State the blood parasite species.
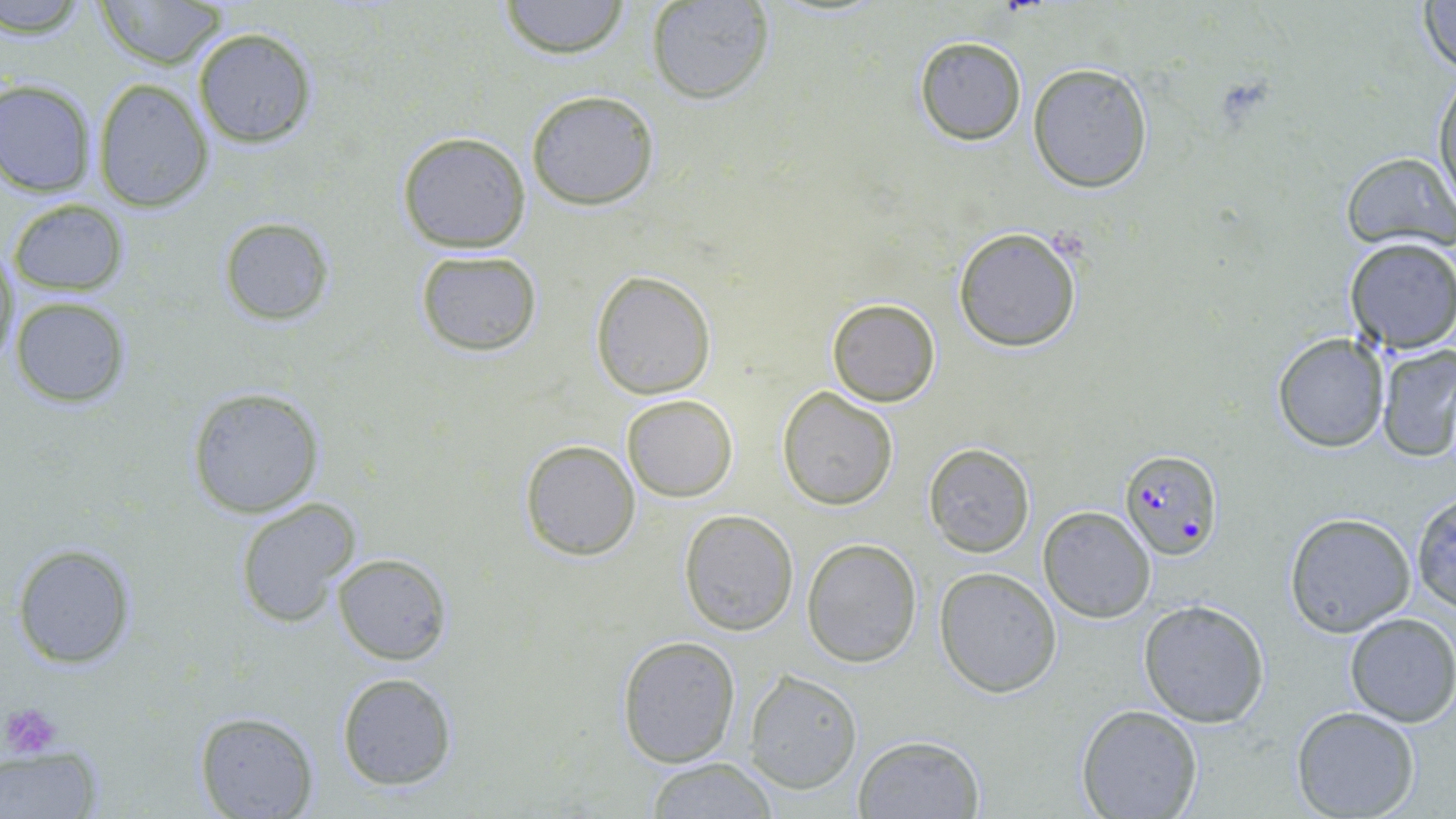

Plasmodium falciparum.

Approximate bounding boxes as (x1, y1, x2, y2) in pixels. Plasmodium falciparum-infected red blood cell locations: (1120, 448, 1224, 558). Platelet locations: (3, 702, 61, 760). Uninfected red blood cell locations: (96, 0, 228, 70), (498, 0, 631, 58), (649, 0, 776, 104), (3, 1, 91, 37), (1418, 1, 1456, 77), (192, 27, 319, 148), (914, 36, 1027, 146), (1028, 63, 1152, 192), (1433, 71, 1456, 212), (93, 79, 214, 211), (0, 80, 96, 196), (524, 90, 661, 210), (396, 130, 531, 253), (1341, 151, 1455, 252), (9, 199, 129, 296), (218, 216, 333, 325), (953, 226, 1082, 352), (1341, 238, 1456, 354), (1, 245, 20, 370), (414, 249, 543, 356), (589, 269, 716, 398), (9, 296, 132, 407), (826, 298, 941, 406), (1272, 332, 1391, 453), (1378, 344, 1456, 463), (186, 386, 323, 518), (776, 386, 899, 511), (621, 394, 737, 501), (518, 439, 641, 562), (922, 443, 1035, 558), (1410, 490, 1456, 615), (232, 496, 360, 629), (1038, 506, 1155, 623), (678, 509, 798, 634), (1284, 512, 1415, 637), (803, 539, 922, 667), (11, 543, 136, 668), (333, 553, 451, 664), (934, 567, 1062, 697), (1138, 598, 1270, 726), (1343, 612, 1456, 727), (616, 635, 742, 767), (744, 670, 862, 792), (335, 672, 457, 791), (1075, 703, 1203, 818), (1290, 705, 1420, 819), (194, 711, 319, 819), (852, 734, 985, 818), (0, 748, 103, 817), (643, 757, 779, 818). Image is 1456×819 pixels. Light microscopy. May-Grünwald-Giemsa-stained preparation. One field of a larger specimen. Thin blood film. Captured at 1000x magnification.